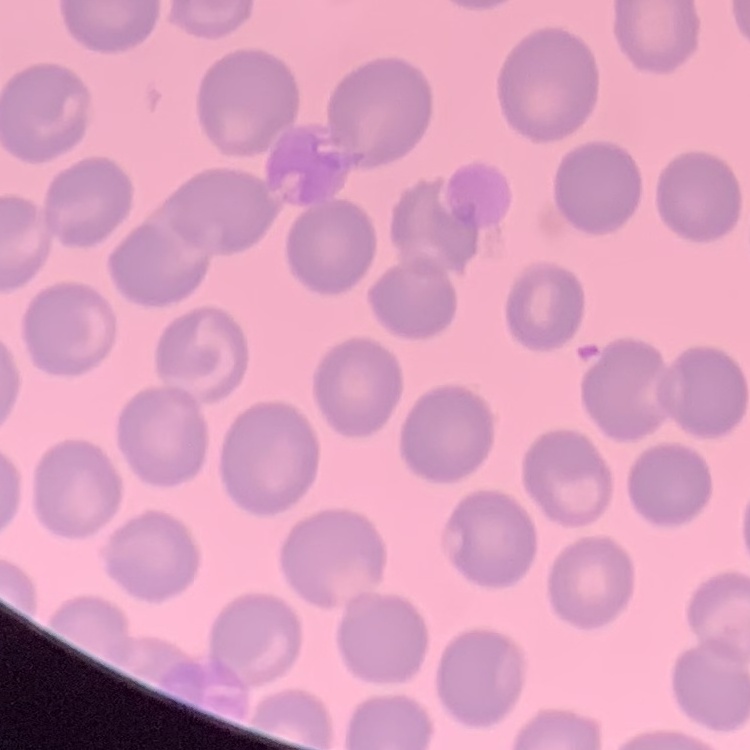

The erythrocytes show no rouleaux formation. One tile cut from a larger photomicrograph. Stained with either Field's or Giemsa. Thin peripheral smear.